Locate every Plasmodium ovale-infected red blood cell.
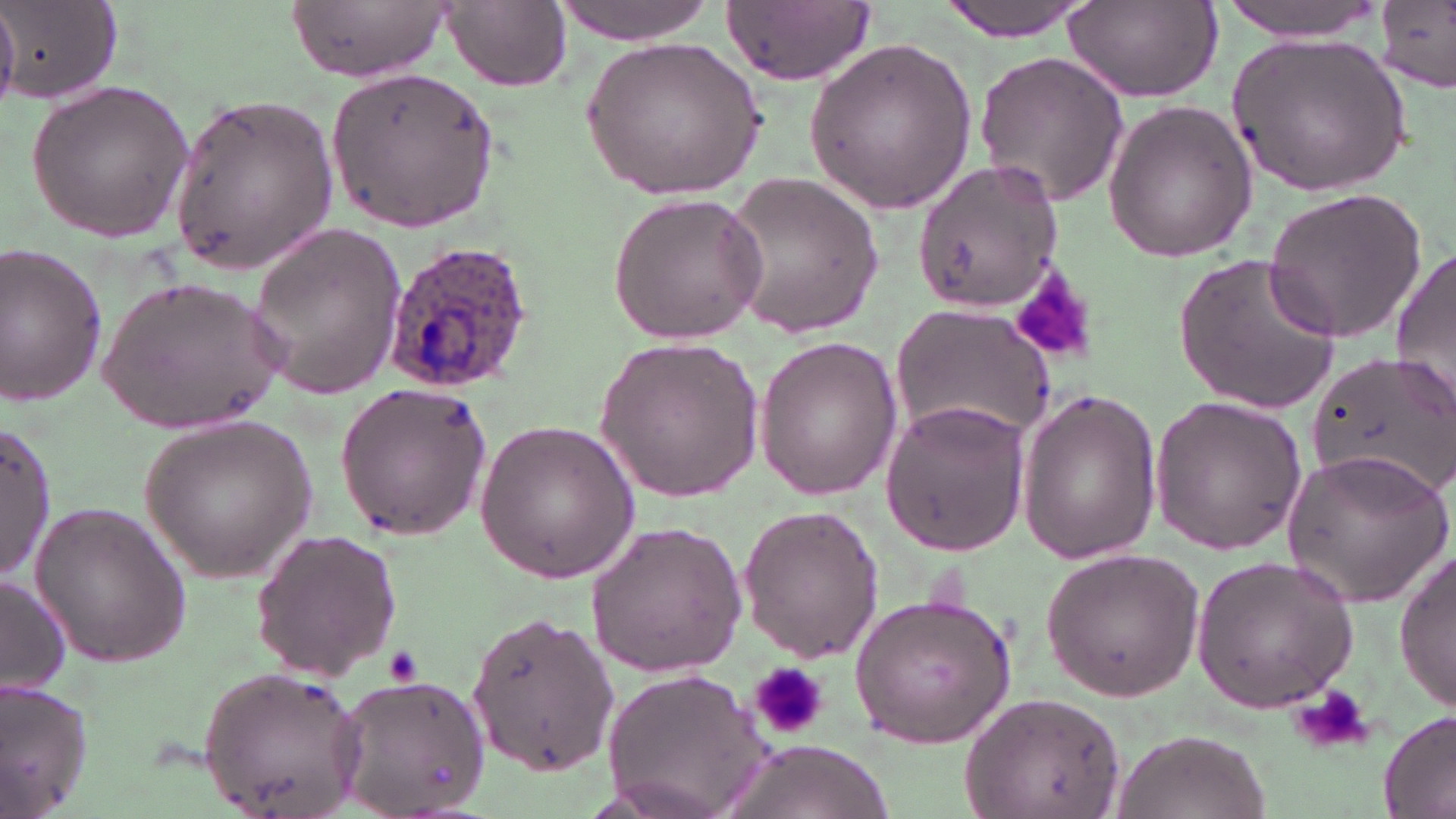

Approximate bounding boxes as (x1,y1)-(x2,y2) corner pairs in pixels.
Plasmodium ovale-infected red blood cells: (381,240)-(536,393).

Platelet locations: (1014,271)-(1101,366), (381,647)-(426,689), (746,660)-(834,740), (1293,680)-(1376,752). Uninfected red blood cell locations: (287,0)-(455,83), (552,0)-(713,45), (721,0)-(877,84), (933,0)-(1103,41), (1217,0)-(1390,39), (1378,1)-(1455,92), (0,3)-(122,107), (443,3)-(571,91), (1061,4)-(1221,103), (1228,27)-(1415,197), (583,35)-(765,202), (802,36)-(976,215), (972,51)-(1132,208), (323,62)-(501,235), (26,77)-(196,244), (168,91)-(337,277), (1100,99)-(1257,264), (912,160)-(1064,314), (723,169)-(884,340), (1264,186)-(1432,344), (606,192)-(767,346), (246,221)-(409,399), (0,246)-(109,405), (1390,247)-(1456,415), (1175,251)-(1342,415), (99,277)-(286,435), (890,303)-(1056,442), (752,335)-(904,499), (595,336)-(766,502), (1307,349)-(1456,498), (335,383)-(493,539), (1015,386)-(1163,564), (1147,395)-(1309,555), (879,397)-(1033,555), (138,414)-(319,581), (474,419)-(639,587), (1,421)-(55,582), (1281,447)-(1452,608), (29,499)-(192,666), (735,502)-(885,662), (584,521)-(748,677), (250,527)-(403,682), (1038,545)-(1208,700), (1394,549)-(1455,711), (1190,553)-(1359,716), (0,573)-(73,696), (848,591)-(1019,749), (463,606)-(618,773), (598,666)-(777,819), (196,668)-(366,817), (330,671)-(493,816), (0,678)-(98,819), (960,693)-(1126,814), (1377,707)-(1456,819), (1106,726)-(1271,819), (721,743)-(895,819). Slide-level diagnosis: Plasmodium ovale. Light microscopy. May-Grünwald-Giemsa-stained preparation. Image is 1456×819 pixels. Thin blood smear. Captured at 1000x magnification. One field of a larger specimen.